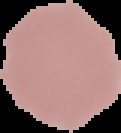
Image is 121×133 pixels. Cell region segmented out of the field of view; the surrounding area is masked to black. Malaria status: uninfected. From a thin blood smear.